State which parasite is depicted.
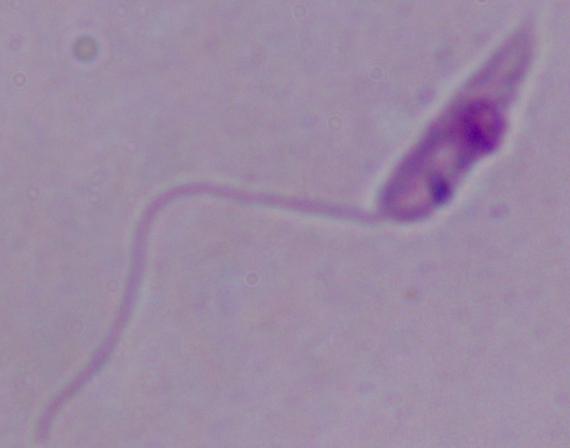
This is Leishmania.

Micrograph. 1000x magnification.